Identify the parasite.
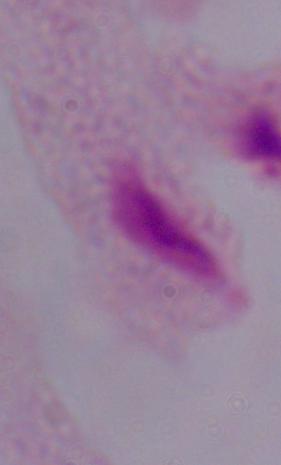

A trichomonad.

modality = photomicrograph
magnification = 1000x